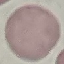

malaria_status: uninfected
stain: Giemsa
image_type: automatically extracted cell patch, resized to 64 × 64 pixels
preparation: thin blood smear
capture: smartphone through the microscope eyepiece